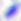
Summary:
  - Magnification: 400x
  - Modality: micrograph
  - Identification: Toxoplasma gondii